Report the malaria status of this cell.
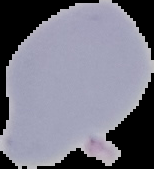

It is uninfected.

Image is 154×169 pixels. From a thin blood smear. The area outside the segmented cell region is set to black.